Identify the cell.
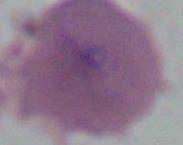

An erythrocyte.

magnification = 1000x
modality = micrograph